Describe the morphology of the erythrocytes.
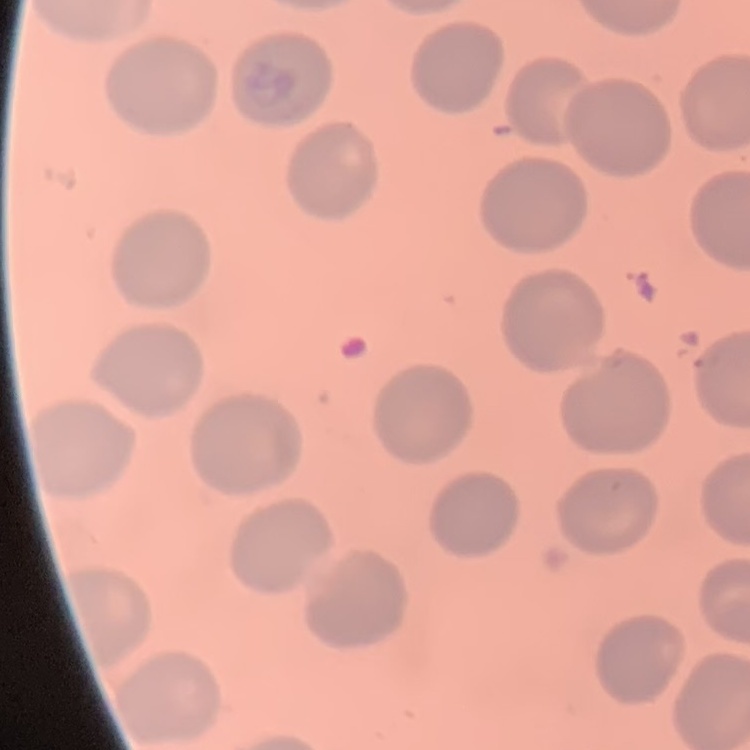
They show no rouleaux formation.

Summary:
  - Stain: Field's or Giemsa
  - Image type: one tile cut from a larger photomicrograph
  - Preparation: thin blood film